Report the malaria status of this cell.
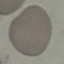

It is uninfected.

stain: Giemsa
preparation: thin smear
capture: smartphone camera at the microscope eyepiece
image_type: automatically extracted cell patch, resized to 64 × 64 pixels